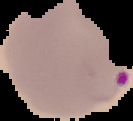
Result: malaria parasites detected. Image is 133×121 pixels. From a thin blood film. Segmented cell region on a black background.